Name the cell type shown.
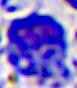
A leukocyte.

Captured at 400x magnification. Photomicrograph.